Describe the morphology of the erythrocytes.
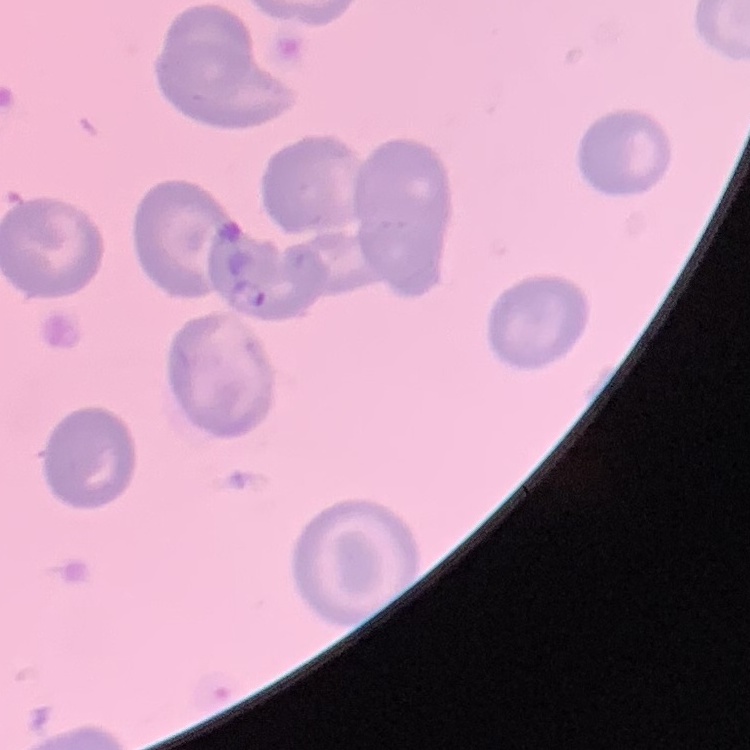

No rouleaux formation.

{
  "image_type": "square crop of a larger photomicrograph",
  "preparation": "thin blood smear",
  "stain": "Field's or Giemsa"
}